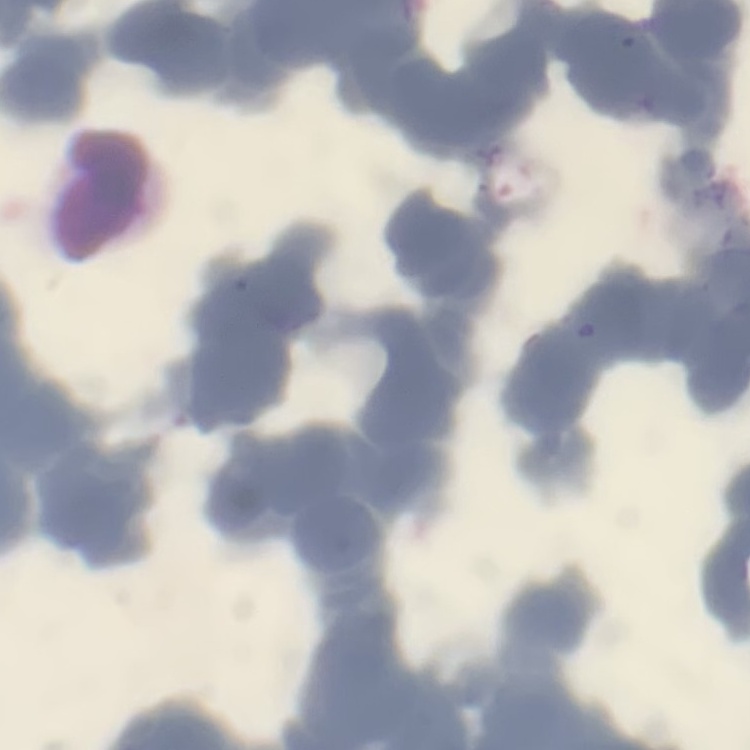 The erythrocytes show rouleaux formation. One tile cut from a larger photomicrograph. Thin blood smear. Stained with either Field's or Giemsa.